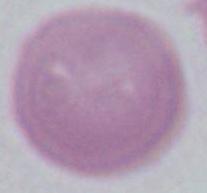

Photomicrograph. 1000x magnification. A red blood cell is shown.